Locate and identify every blood parasite.
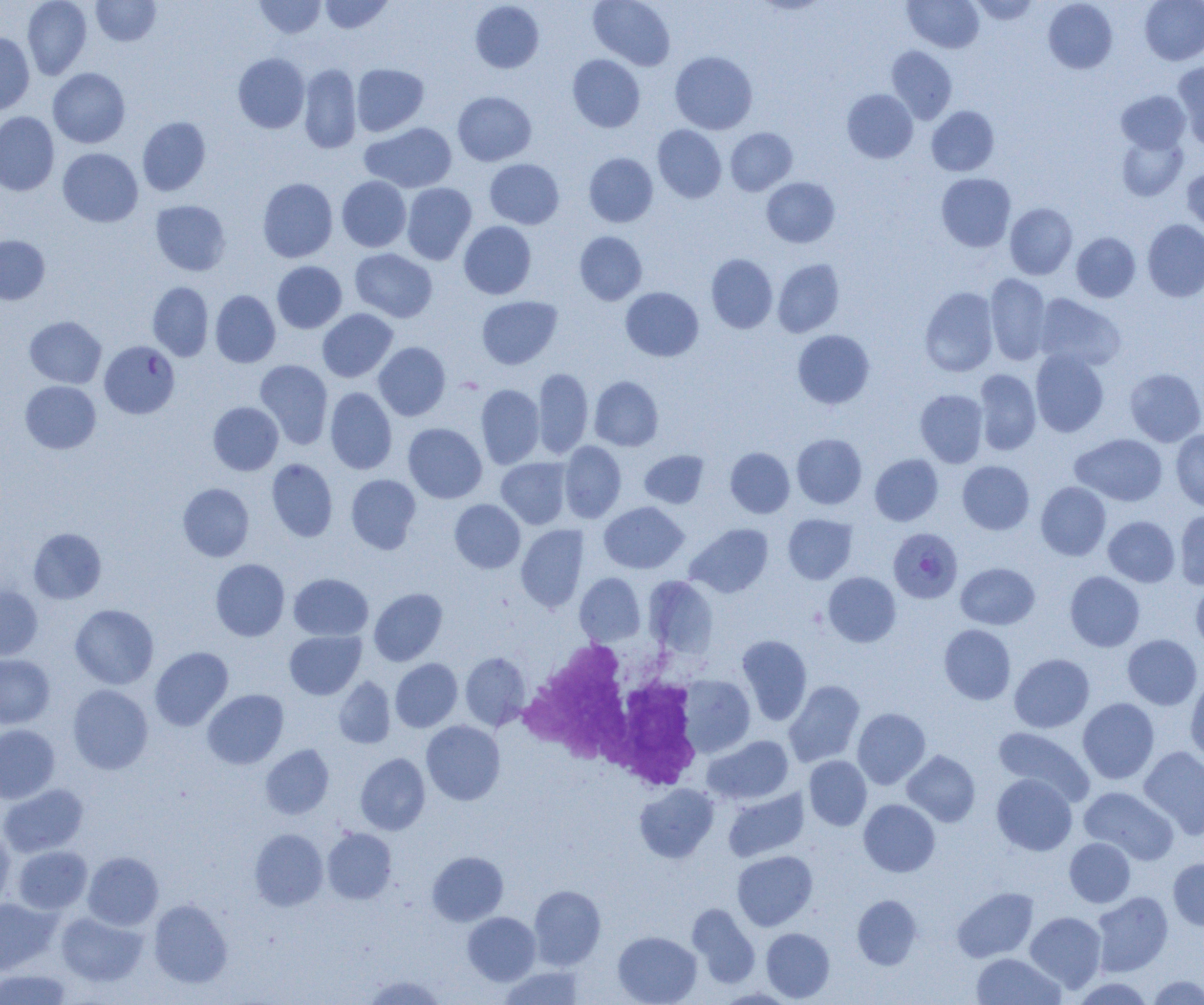

Approximate bounding boxes as (x1, y1, x2, y2) in pixels.
Plasmodium falciparum-infected red blood cells: (99, 341, 179, 419), (888, 527, 963, 603).
No Plasmodium ovale, Plasmodium malariae, Plasmodium vivax, Babesia divergens, or Trypanosoma brucei observed.

Summary:
  - White blood cell locations: (516, 638, 704, 793)
  - Uninfected red blood cell locations: (22, 0, 92, 80), (91, 0, 160, 46), (255, 0, 326, 38), (319, 0, 393, 34), (588, 0, 676, 70), (903, 0, 984, 53), (969, 0, 1041, 24), (1043, 0, 1118, 74), (1140, 0, 1204, 65), (470, 1, 544, 74), (0, 32, 35, 115), (886, 46, 957, 123), (669, 51, 757, 134), (233, 53, 309, 133), (567, 55, 645, 132), (1173, 62, 1204, 149), (298, 64, 362, 154), (351, 64, 429, 136), (48, 68, 130, 148), (842, 89, 918, 163), (453, 91, 536, 166), (1116, 91, 1190, 153), (927, 106, 998, 176), (0, 112, 59, 195), (137, 117, 211, 196), (361, 122, 457, 193), (652, 125, 726, 203), (725, 127, 797, 195), (1116, 132, 1188, 201), (58, 148, 143, 227), (584, 153, 658, 227), (485, 159, 563, 229), (1182, 167, 1204, 239), (936, 173, 1016, 252), (337, 176, 411, 252), (761, 177, 839, 248), (257, 178, 338, 262), (402, 183, 477, 264), (150, 200, 231, 276), (1005, 203, 1077, 279), (1142, 219, 1204, 301), (459, 221, 537, 299), (574, 231, 647, 305), (1071, 232, 1140, 302), (0, 235, 50, 305), (350, 248, 437, 322), (706, 254, 778, 333), (773, 259, 844, 337), (272, 261, 347, 333), (985, 273, 1052, 365), (147, 282, 213, 361), (621, 287, 703, 361), (920, 287, 999, 376), (210, 290, 280, 368), (1034, 294, 1126, 371), (477, 296, 562, 369), (317, 308, 398, 382), (24, 316, 106, 388), (792, 330, 875, 409), (373, 342, 450, 421), (1030, 349, 1109, 437), (255, 360, 333, 449), (532, 367, 593, 458), (1124, 367, 1204, 446), (973, 369, 1041, 455), (589, 376, 663, 451), (20, 381, 101, 453), (476, 384, 544, 468), (325, 387, 397, 474), (915, 389, 988, 467), (208, 402, 283, 475), (403, 423, 487, 503), (1170, 428, 1204, 511), (792, 433, 867, 509), (1070, 433, 1167, 506), (559, 441, 627, 523), (725, 447, 795, 518), (639, 450, 709, 508), (870, 454, 943, 526), (496, 457, 571, 529), (266, 458, 338, 542), (957, 460, 1035, 535), (345, 474, 421, 554), (1035, 482, 1111, 560), (178, 483, 254, 561), (449, 499, 525, 573), (599, 501, 688, 574), (1175, 509, 1204, 590), (783, 514, 857, 584), (1103, 515, 1180, 587), (685, 523, 773, 597), (516, 524, 589, 612), (28, 527, 106, 604), (210, 559, 290, 641), (956, 562, 1039, 630), (1065, 571, 1145, 651), (823, 572, 901, 647), (289, 573, 373, 641), (574, 573, 646, 646), (643, 575, 719, 659), (1191, 578, 1204, 655), (0, 585, 43, 660), (369, 588, 447, 666), (70, 604, 159, 689), (939, 624, 1016, 704), (284, 630, 365, 700), (736, 634, 812, 726), (1122, 634, 1202, 710), (150, 647, 233, 731), (460, 652, 531, 730), (1009, 653, 1094, 732), (0, 654, 55, 728), (390, 658, 462, 732), (678, 674, 755, 757), (334, 676, 395, 749), (1185, 676, 1204, 764), (783, 680, 865, 767), (67, 685, 153, 774), (202, 689, 288, 769), (1077, 697, 1159, 784), (852, 708, 930, 789), (421, 720, 505, 805), (0, 724, 59, 803), (993, 727, 1094, 805), (705, 735, 794, 803), (261, 744, 334, 819), (1138, 746, 1204, 838), (902, 750, 980, 827), (355, 753, 430, 835), (804, 756, 872, 830), (991, 773, 1077, 855), (0, 783, 88, 857), (634, 783, 719, 863), (1079, 786, 1178, 865), (723, 788, 809, 861), (859, 799, 940, 877), (0, 827, 15, 908), (322, 827, 397, 904), (250, 829, 328, 911), (1064, 838, 1135, 908), (12, 845, 92, 914), (732, 850, 817, 930), (427, 851, 508, 925), (83, 852, 163, 930), (1168, 858, 1204, 930), (529, 885, 606, 969), (952, 887, 1039, 962), (1091, 891, 1173, 976), (852, 894, 922, 970), (0, 898, 59, 974), (149, 899, 232, 987), (687, 903, 760, 988), (56, 911, 147, 986), (1025, 911, 1106, 992), (463, 912, 540, 985), (761, 928, 835, 1002), (612, 931, 701, 1005), (972, 952, 1065, 1005), (498, 965, 587, 1004), (0, 969, 74, 1005), (363, 974, 447, 1005), (1146, 975, 1203, 1004), (1070, 977, 1156, 1004)
  - Slide-level diagnosis: Plasmodium falciparum
  - Magnification: 1000x
  - Image size: 1204×1005 pixels
  - Preparation: thin blood smear
  - Field of view: one of a larger specimen
  - Modality: optical microscopy